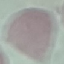
Malaria status: uninfected. Giemsa-stained preparation. Thin blood smear. Cell patch, automatically extracted from a larger field of view and resized to 64 × 64 pixels. Acquired by smartphone through the microscope eyepiece.